Locate every Plasmodium parasite.
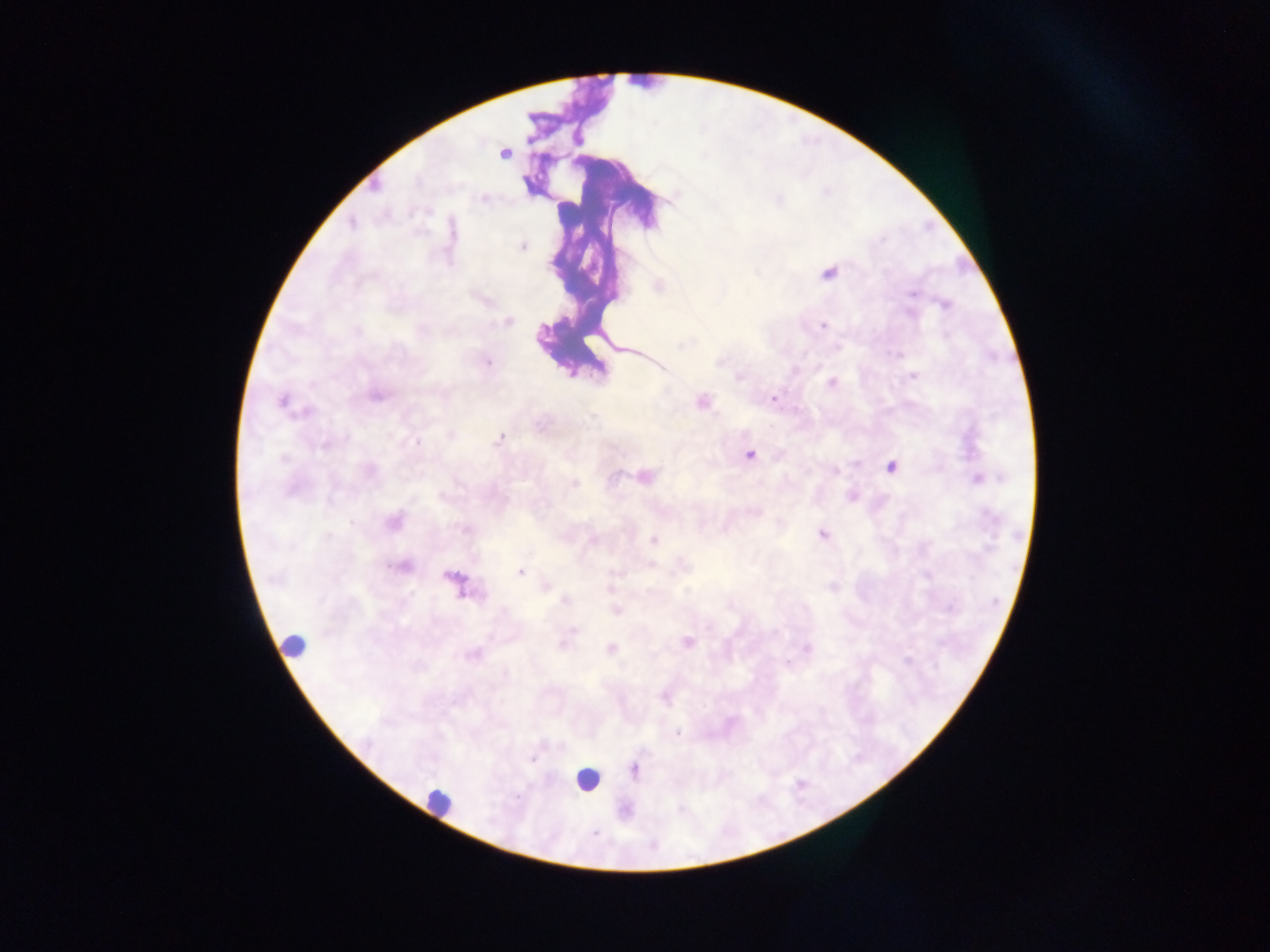
Approximate centers as [x, y] in pixels.
Plasmodium parasites: [504, 155], [375, 186], [483, 198], [779, 199], [351, 224], [882, 239], [522, 246], [551, 265], [829, 274], [911, 294], [945, 305], [909, 314], [507, 322], [823, 325], [358, 331], [682, 344], [836, 348], [897, 355], [721, 362], [488, 363], [795, 371], [913, 376], [739, 377], [831, 383], [376, 396], [773, 398], [282, 401], [701, 401], [308, 412], [592, 417], [450, 434], [500, 439], [417, 442], [324, 445], [749, 455], [283, 459], [891, 467], [370, 471], [834, 472], [614, 477], [646, 477], [978, 478], [574, 484], [852, 496], [393, 522], [464, 529], [823, 534], [327, 537], [592, 540], [653, 540], [650, 564], [402, 566], [520, 573], [926, 575], [452, 578], [831, 586], [545, 587], [610, 588], [566, 601], [950, 608], [616, 611], [575, 630], [686, 642], [562, 644], [807, 648], [611, 649], [473, 654], [907, 660], [677, 733], [533, 760], [634, 770].

Leukocyte locations: [568, 211], [286, 641], [586, 779], [440, 800]. Collected in Ghana. One field of view. Photographed through a microscope with a mobile-phone camera. Thick blood film. Image is 1270×952 pixels.